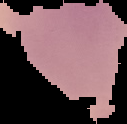

Summary:
  - Image type: cell region segmented out of the field of view; surrounding area masked to black
  - Malaria status: parasitized
  - Preparation: thin blood smear
  - Image size: 127×124 pixels